Locate every uninfected red blood cell.
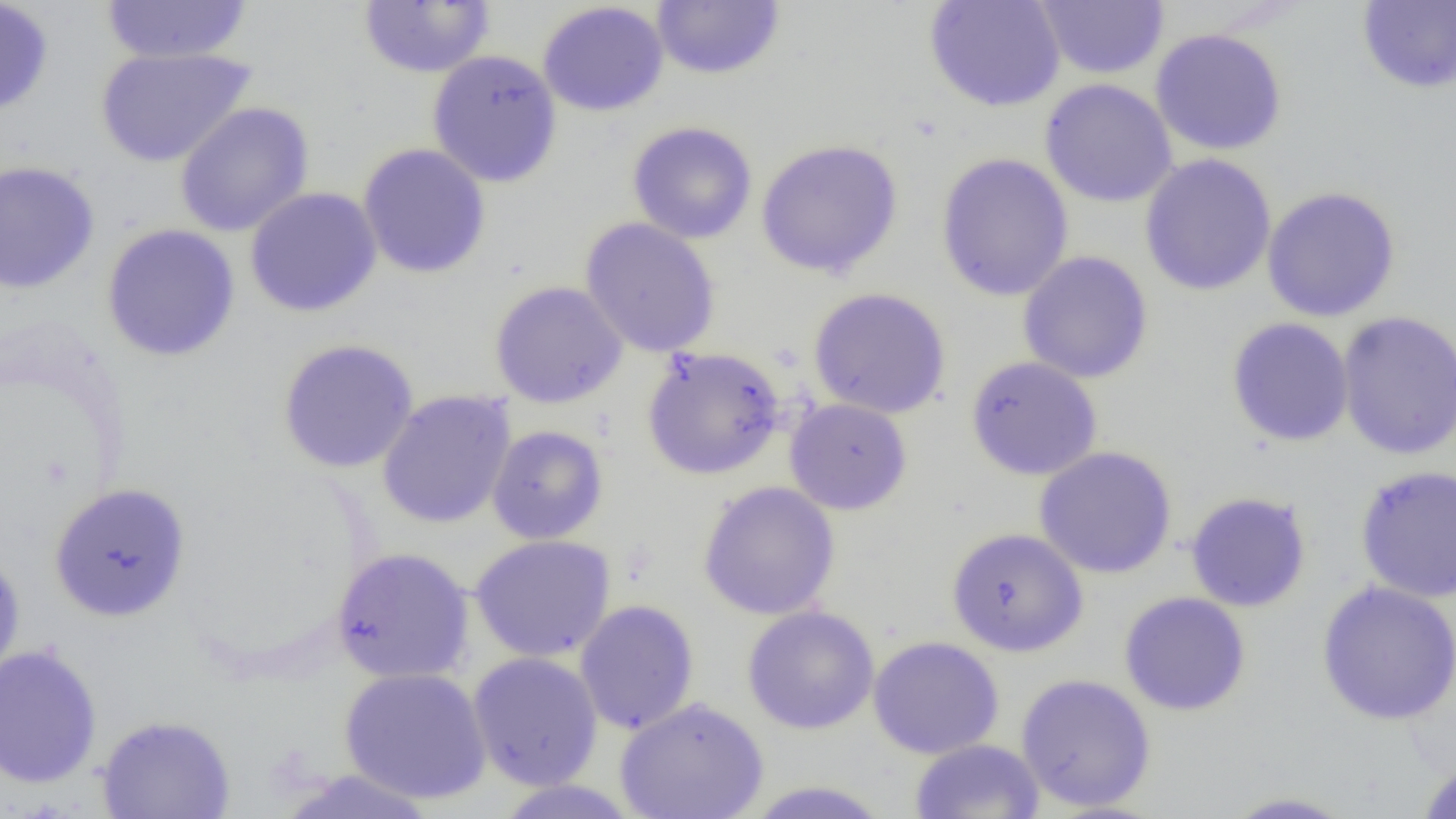
Approximate bounding boxes as [x1, y1, x2, y2] in pixels.
Uninfected red blood cells: [0, 0, 54, 117], [100, 0, 254, 65], [651, 0, 785, 80], [924, 0, 1066, 112], [1034, 0, 1170, 80], [359, 1, 495, 78], [537, 1, 669, 117], [1356, 1, 1456, 94], [1149, 28, 1288, 156], [93, 46, 257, 168], [426, 49, 563, 187], [1039, 79, 1177, 208], [174, 102, 314, 237], [627, 121, 758, 244], [756, 138, 903, 278], [357, 143, 492, 279], [935, 152, 1074, 302], [1139, 153, 1277, 297], [0, 159, 101, 294], [1261, 185, 1401, 322], [244, 187, 383, 318], [579, 217, 721, 358], [101, 223, 241, 362], [1017, 250, 1154, 384], [489, 280, 628, 409], [808, 287, 951, 419], [1337, 309, 1456, 461], [1226, 317, 1355, 447], [277, 339, 419, 474], [642, 346, 785, 480], [965, 355, 1103, 481], [377, 390, 516, 529], [785, 398, 912, 515], [487, 424, 609, 544], [1034, 446, 1177, 579], [1354, 465, 1456, 602], [698, 481, 840, 620], [49, 482, 191, 622], [1185, 491, 1312, 612], [946, 527, 1088, 657], [470, 534, 616, 663], [331, 547, 475, 685], [0, 548, 26, 684], [1316, 580, 1456, 725], [1119, 591, 1251, 716], [574, 599, 699, 735], [742, 605, 880, 734], [867, 636, 1004, 759], [0, 643, 103, 790], [467, 651, 604, 791], [339, 666, 492, 804], [1015, 673, 1157, 812], [614, 696, 769, 819], [96, 714, 237, 819], [909, 738, 1045, 819], [1415, 760, 1456, 819], [274, 769, 441, 818], [491, 779, 644, 819], [740, 781, 895, 818], [1218, 790, 1362, 818].

Slide-level diagnosis: no evidence of blood parasites. Image is 1456×819 pixels. Single field of view. 1000x magnification. Optical microscopy. Thin blood smear.